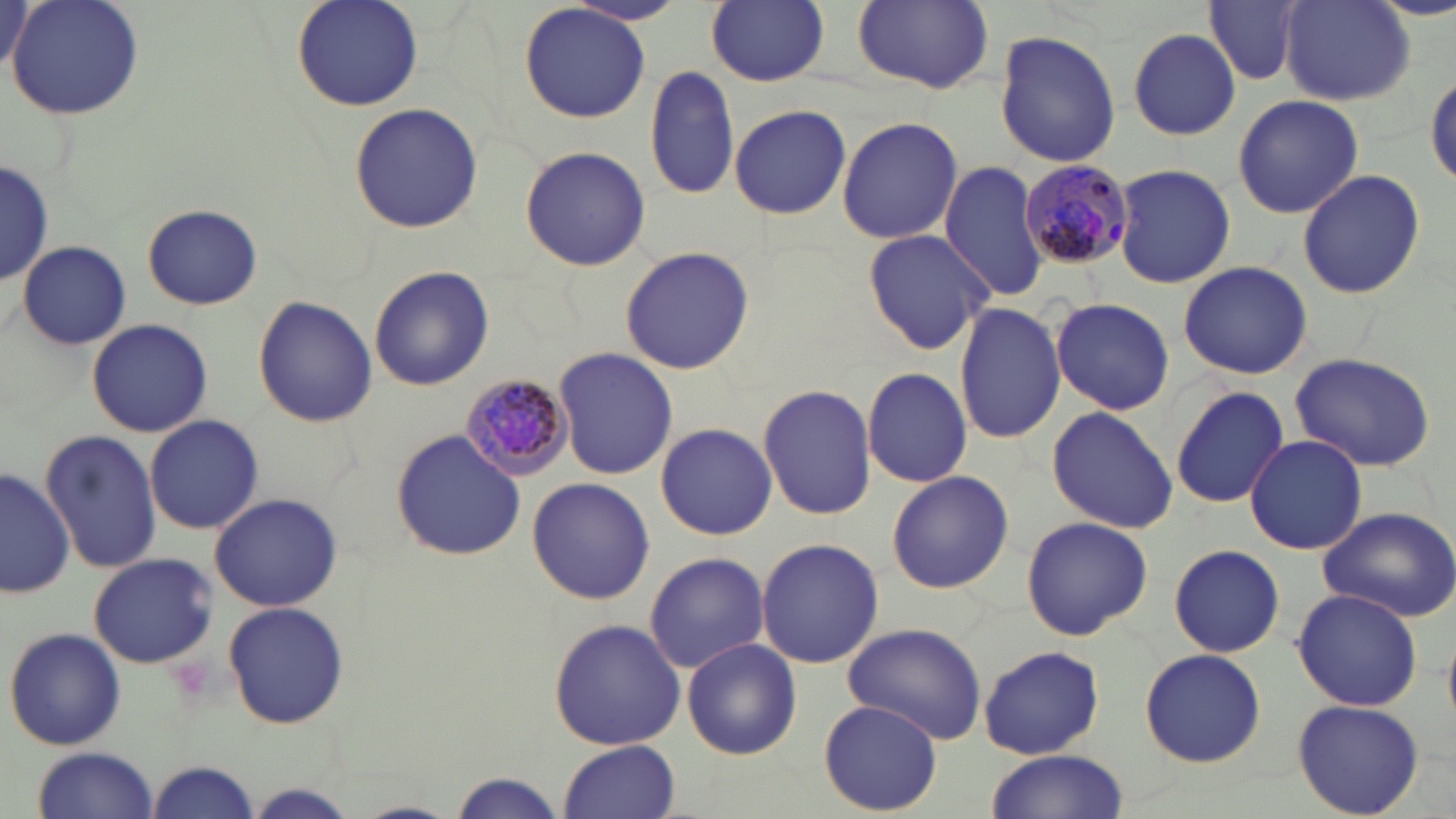

Approximate bounding boxes as (x1, y1, x2, y2) in pixels. Uninfected red blood cell locations: (2, 0, 32, 77), (8, 0, 145, 120), (292, 0, 423, 112), (706, 0, 829, 87), (566, 1, 689, 27), (850, 1, 992, 92), (1202, 1, 1307, 86), (1280, 1, 1416, 106), (519, 3, 653, 123), (1129, 29, 1241, 138), (994, 30, 1121, 166), (645, 63, 740, 199), (1427, 69, 1456, 188), (1233, 95, 1363, 217), (349, 102, 483, 233), (730, 103, 851, 219), (837, 116, 963, 246), (520, 145, 652, 271), (0, 155, 51, 283), (939, 159, 1050, 301), (1110, 164, 1237, 287), (1296, 169, 1426, 300), (142, 204, 262, 309), (862, 228, 995, 355), (19, 240, 131, 348), (618, 246, 754, 376), (1178, 261, 1312, 379), (368, 265, 494, 392), (253, 295, 377, 429), (1050, 297, 1174, 416), (954, 303, 1065, 443), (86, 318, 214, 438), (554, 348, 677, 479), (1288, 351, 1438, 471), (861, 367, 972, 488), (758, 384, 875, 519), (1170, 384, 1289, 509), (1047, 406, 1177, 535), (146, 416, 263, 535), (655, 423, 777, 540), (40, 427, 160, 575), (392, 429, 526, 562), (1244, 434, 1367, 554), (0, 465, 71, 600), (886, 469, 1014, 593), (525, 478, 657, 606), (208, 492, 342, 611), (1317, 506, 1456, 623), (1020, 515, 1153, 641), (756, 537, 884, 669), (1169, 543, 1285, 658), (643, 552, 770, 674), (86, 553, 220, 669), (1292, 589, 1424, 713), (223, 600, 349, 730), (548, 618, 687, 751), (842, 623, 988, 745), (4, 627, 126, 751), (680, 638, 802, 759), (978, 646, 1105, 758), (1137, 648, 1268, 767), (819, 699, 944, 816), (1291, 700, 1425, 817), (558, 740, 680, 819), (30, 746, 159, 819), (981, 751, 1130, 819), (149, 761, 260, 817), (448, 774, 567, 818), (243, 783, 356, 818), (349, 801, 463, 819). Plasmodium malariae-infected red blood cell locations: (1020, 158, 1137, 271), (459, 370, 575, 483). Slide-level diagnosis: Plasmodium malariae. 1000x magnification. Light microscopy. May-Grünwald-Giemsa-stained preparation. Thin blood film. Image is 1456×819 pixels. One field of a larger specimen.